Name the blood parasite species.
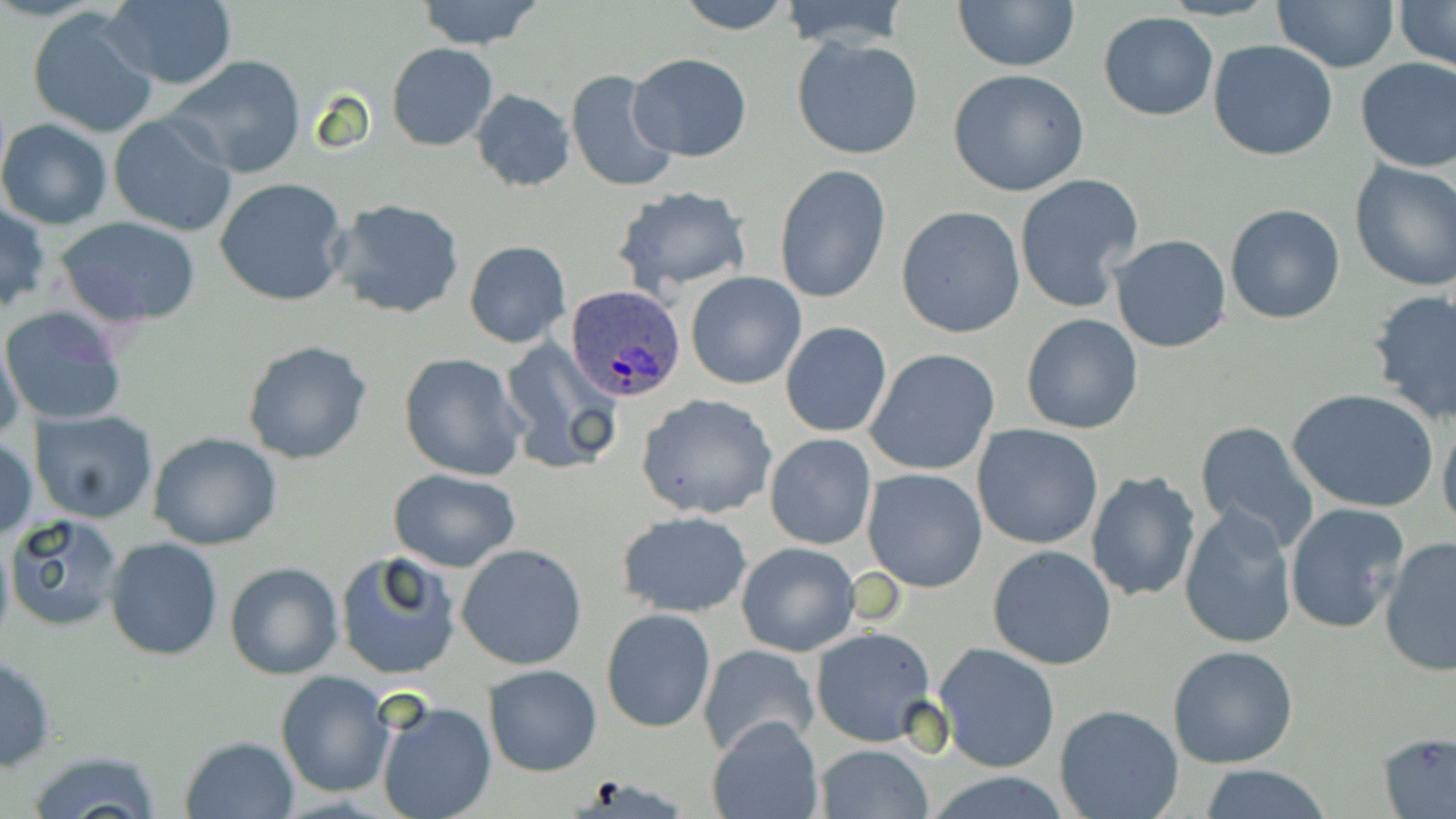
Plasmodium ovale.

uninfected red blood cell locations = approximate bounding boxes as (x1, y1, x2, y2) in pixels: (415, 0, 545, 49), (674, 0, 796, 35), (778, 0, 911, 50), (951, 0, 1080, 71), (1396, 0, 1456, 70), (101, 1, 237, 89), (1273, 1, 1398, 71), (27, 7, 160, 139), (1098, 12, 1220, 121), (793, 37, 924, 161), (1208, 40, 1339, 161), (387, 43, 497, 152), (626, 53, 752, 161), (165, 55, 308, 179), (1354, 57, 1456, 173), (564, 67, 680, 196), (948, 69, 1092, 197), (471, 89, 576, 192), (109, 114, 238, 239), (0, 119, 112, 230), (1349, 160, 1456, 290), (773, 164, 890, 306), (1014, 174, 1143, 313), (214, 178, 349, 306), (611, 186, 752, 295), (328, 198, 468, 321), (0, 201, 49, 314), (1224, 203, 1346, 324), (896, 205, 1025, 339), (57, 217, 203, 329), (1109, 234, 1232, 352), (464, 240, 570, 348), (686, 272, 807, 390), (1367, 289, 1456, 425), (1, 306, 128, 427), (1021, 313, 1145, 435), (780, 321, 893, 437), (1, 332, 26, 448), (242, 340, 373, 465), (499, 340, 621, 475), (866, 348, 1000, 475), (398, 352, 527, 481), (1287, 388, 1439, 513), (638, 392, 778, 519), (30, 411, 159, 525), (1439, 415, 1456, 537), (1194, 420, 1319, 550), (972, 423, 1103, 549), (764, 432, 878, 550), (149, 433, 283, 551), (1, 438, 37, 542), (866, 443, 1089, 574), (388, 468, 521, 571), (862, 468, 988, 593), (1085, 469, 1201, 603), (1284, 502, 1409, 635), (1178, 505, 1298, 649), (616, 510, 753, 617), (5, 512, 127, 631), (104, 536, 225, 661), (1380, 537, 1456, 676), (736, 541, 861, 657), (456, 545, 587, 668), (986, 545, 1117, 670), (333, 552, 462, 682), (224, 560, 342, 679), (601, 608, 716, 733), (810, 627, 937, 747), (933, 643, 1061, 773), (697, 644, 820, 760), (1166, 644, 1299, 769), (0, 654, 56, 773), (482, 665, 602, 776), (276, 672, 396, 795), (375, 697, 496, 819), (1054, 703, 1183, 819), (707, 715, 823, 819), (1378, 732, 1456, 818), (179, 735, 298, 818), (813, 745, 935, 819), (24, 749, 162, 819), (1195, 766, 1333, 819), (927, 772, 1075, 818)
field of view = single
image size = 1456×819 pixels
modality = light microscopy
magnification = 1000x
preparation = thin blood film
stain = May-Grünwald-Giemsa
Plasmodium ovale-infected red blood cell locations = approximate bounding boxes as (x1, y1, x2, y2) in pixels: (567, 285, 686, 401)